Locate and identify every blood parasite.
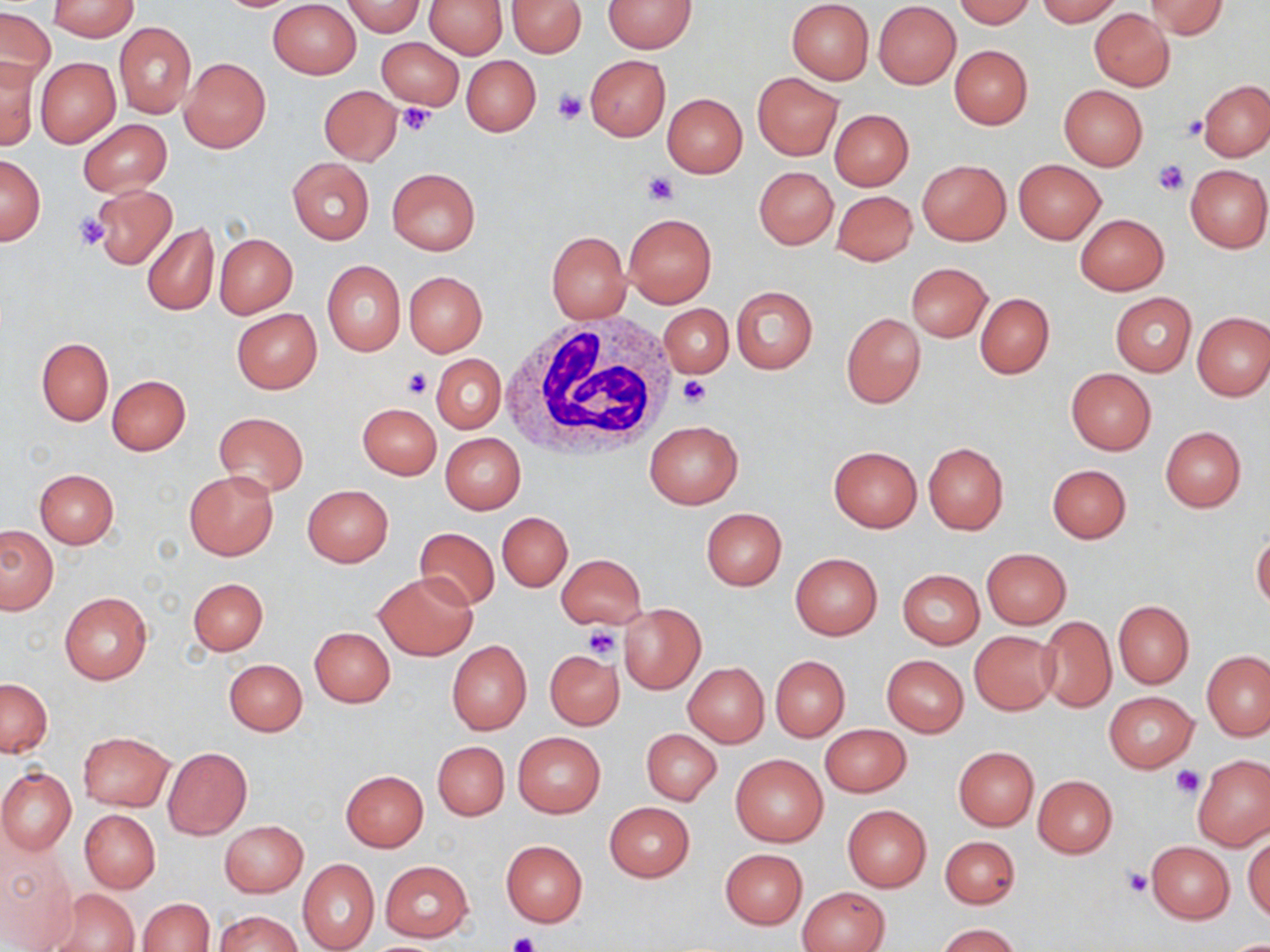

No blood parasites seen.

Summary:
  - Coordinate format: approximate bounding boxes as [x1, y1, x2, y2] in pixels
  - Uninfected red blood cell locations: [49, 0, 137, 40], [425, 0, 507, 58], [507, 0, 585, 57], [604, 0, 697, 52], [952, 0, 1034, 27], [1036, 0, 1123, 25], [1146, 0, 1228, 39], [268, 1, 362, 79], [340, 1, 425, 36], [786, 1, 874, 84], [874, 2, 960, 89], [1, 8, 56, 86], [1088, 9, 1174, 91], [114, 21, 196, 119], [376, 35, 464, 113], [949, 44, 1032, 129], [585, 54, 670, 141], [0, 56, 41, 150], [461, 56, 541, 135], [35, 57, 120, 147], [180, 57, 271, 153], [752, 73, 843, 160], [1199, 79, 1270, 161], [318, 85, 402, 165], [1058, 85, 1148, 171], [661, 92, 747, 178], [829, 108, 913, 190], [77, 119, 172, 195], [0, 154, 44, 245], [287, 158, 375, 244], [918, 159, 1011, 246], [1014, 160, 1106, 243], [1185, 164, 1269, 253], [387, 167, 479, 255], [754, 167, 838, 249], [91, 185, 177, 270], [830, 189, 918, 265], [624, 212, 716, 308], [1075, 214, 1168, 294], [142, 223, 218, 317], [547, 231, 630, 323], [214, 233, 297, 317], [322, 260, 406, 356], [907, 263, 992, 342], [403, 271, 488, 356], [731, 286, 818, 374], [974, 292, 1053, 378], [1110, 293, 1197, 376], [659, 304, 733, 377], [231, 309, 322, 393], [1193, 311, 1270, 400], [841, 312, 926, 408], [36, 338, 113, 425], [431, 354, 506, 434], [1065, 368, 1156, 454], [106, 375, 190, 454], [358, 403, 441, 479], [213, 411, 309, 496], [645, 421, 742, 509], [1160, 427, 1246, 512], [440, 433, 524, 514], [923, 442, 1009, 534], [828, 445, 921, 532], [1047, 464, 1131, 544], [35, 469, 119, 547], [184, 469, 279, 560], [303, 485, 392, 567], [700, 507, 787, 590], [497, 512, 573, 591], [0, 525, 58, 614], [413, 528, 501, 610], [1251, 533, 1270, 613], [981, 548, 1072, 629], [790, 553, 882, 639], [557, 554, 646, 629], [897, 569, 984, 648], [373, 571, 477, 660], [187, 577, 268, 656], [59, 592, 152, 684], [1113, 600, 1194, 688], [619, 603, 706, 694], [1038, 617, 1116, 713], [310, 627, 395, 707], [969, 630, 1060, 714], [447, 640, 532, 734], [544, 649, 624, 730], [1202, 650, 1269, 740], [882, 654, 968, 737], [770, 656, 850, 740], [224, 658, 307, 736], [684, 662, 769, 746], [0, 678, 52, 757], [1105, 690, 1196, 771], [820, 724, 910, 797], [641, 728, 721, 805], [77, 732, 174, 811], [513, 732, 605, 817], [432, 741, 509, 821], [164, 747, 252, 839], [953, 747, 1038, 830], [731, 752, 828, 847], [1193, 755, 1270, 850], [0, 767, 76, 855], [341, 770, 428, 851], [1033, 775, 1117, 857], [604, 802, 695, 882], [842, 806, 932, 892], [79, 809, 161, 893], [220, 820, 308, 896], [1245, 832, 1270, 924], [941, 835, 1021, 910], [500, 840, 588, 927], [1146, 841, 1236, 924], [721, 848, 807, 929], [0, 849, 76, 949], [297, 858, 378, 952], [380, 861, 474, 941], [799, 887, 889, 952], [45, 889, 140, 952], [139, 898, 214, 951], [215, 911, 300, 951], [938, 923, 1020, 952]
  - Platelet locations: [552, 90, 588, 124], [396, 103, 434, 136], [1182, 115, 1207, 142], [1153, 158, 1189, 195], [645, 172, 678, 204], [72, 213, 111, 251], [402, 368, 431, 398], [677, 376, 711, 408], [582, 626, 622, 660], [1171, 765, 1205, 798], [1123, 868, 1153, 897], [506, 932, 541, 952]
  - White blood cell locations: [500, 316, 679, 457]
  - Slide-level diagnosis: negative for blood parasites
  - Stain: May-Grünwald-Giemsa
  - Modality: optical microscopy
  - Magnification: 1000x
  - Image size: 1270×952 pixels
  - Field of view: single
  - Preparation: thin blood smear